Classify this cell by malaria status.
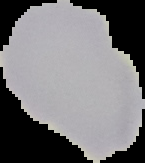

Uninfected.

preparation = thin blood film
image size = 145×163 pixels
image type = segmented cell region with the area outside set to black